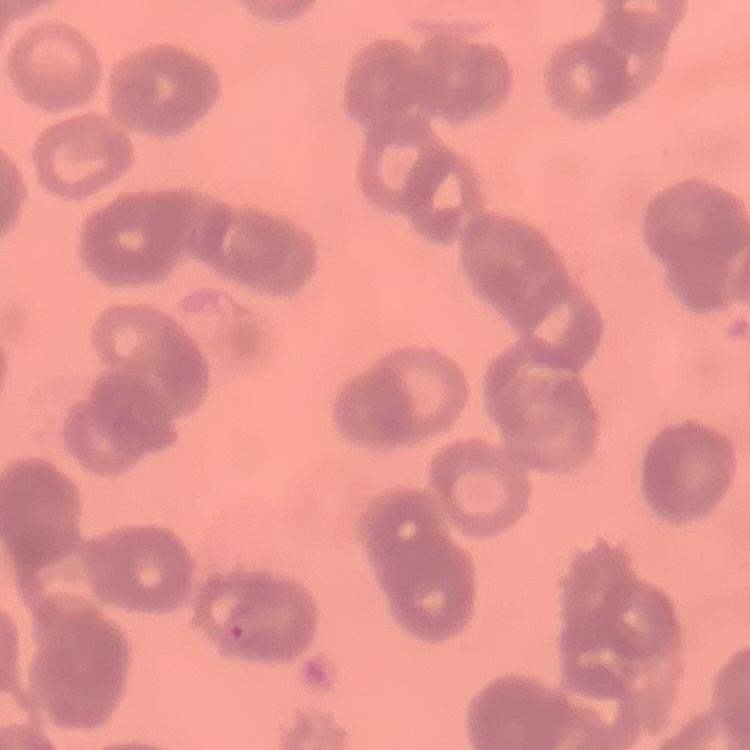
red_blood_cell_morphology: rouleaux formation
preparation: thin blood film
image_type: square crop of a larger photomicrograph
stain: Field's or Giemsa